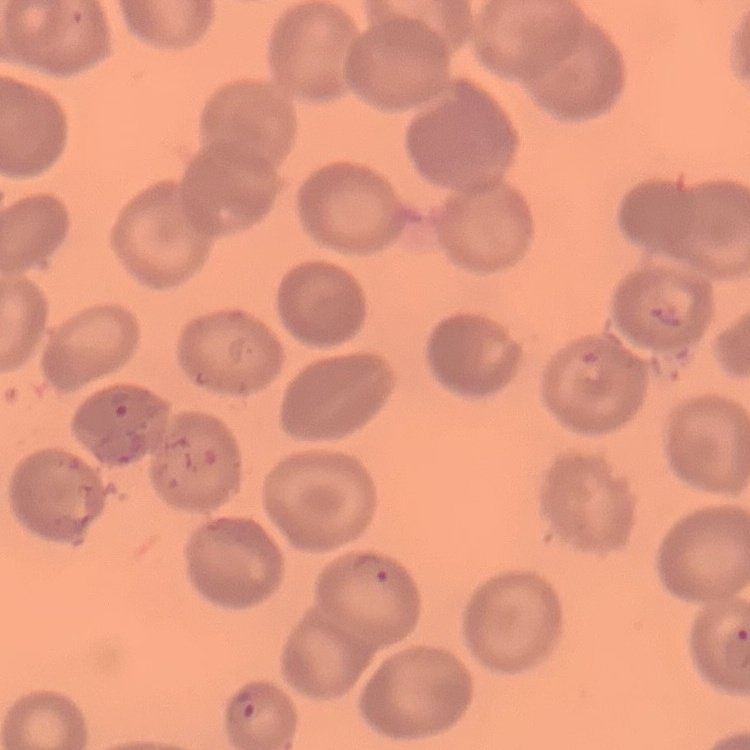 The erythrocytes show no rouleaux formation. Square crop of a larger photomicrograph. Thin blood film. Field's or Giemsa stain.